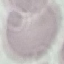
Summary:
  - Malaria status: uninfected
  - Capture: smartphone camera at the microscope eyepiece
  - Stain: Giemsa
  - Preparation: thin blood smear
  - Image type: cell patch, automatically extracted from a larger field of view and resized to 64 × 64 pixels